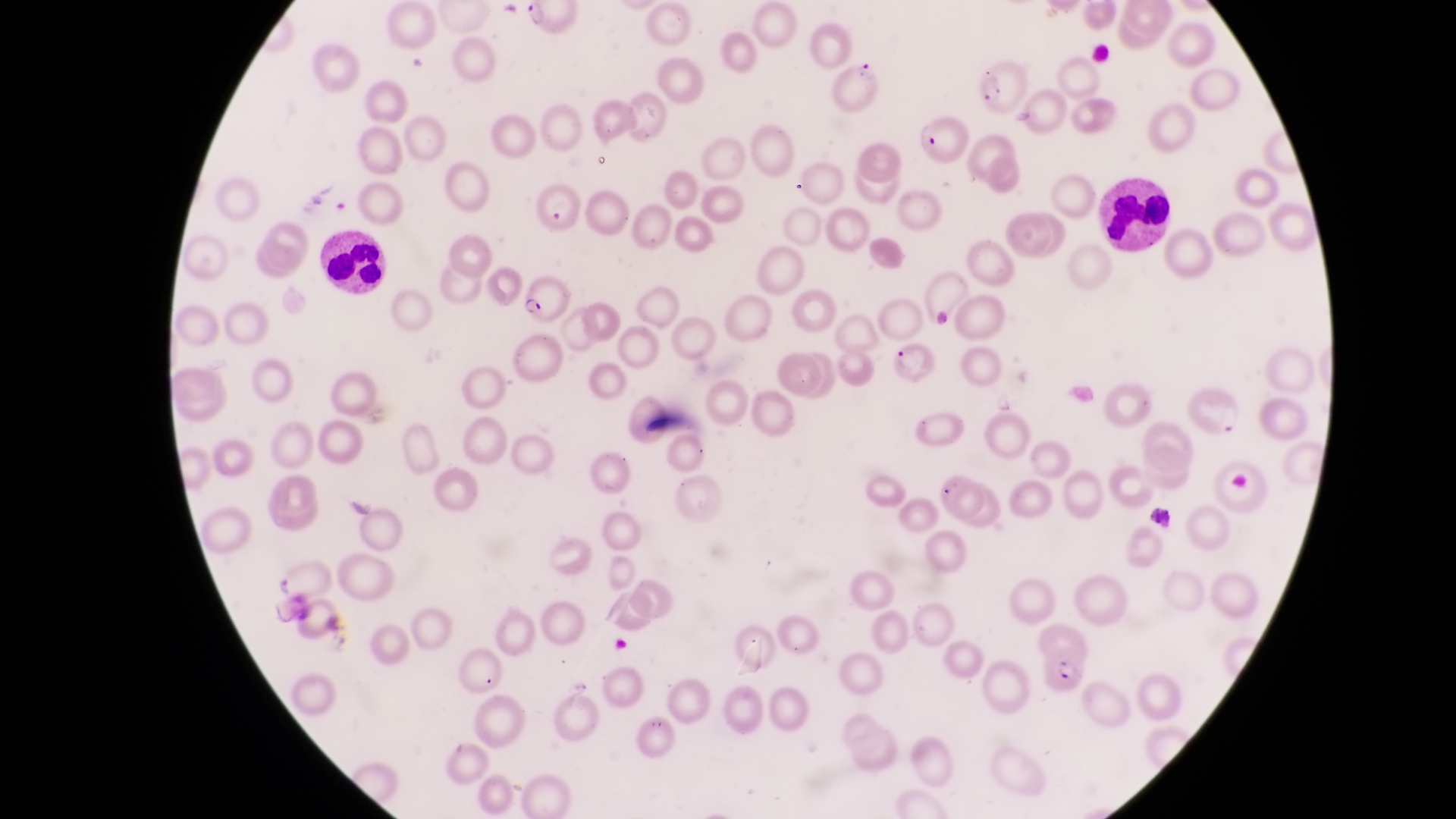
Approximate bounding boxes as (left, top, right, bottom) in pixels. Leukocyte locations: (1100, 174, 1173, 254), (320, 228, 393, 300). Parasitised red blood cell locations: (525, 2, 571, 45), (975, 60, 1027, 112), (835, 64, 887, 119), (915, 115, 971, 162), (535, 182, 582, 237), (526, 274, 566, 323), (886, 340, 950, 395), (1040, 644, 1090, 697). Collected in Uganda. One field of view. Magnification of 1000x. Thin blood film. Image is 1456×819 pixels. Captured by a smartphone held over the eyepiece of an Olympus CX-23 microscope.